Name the cell type shown.
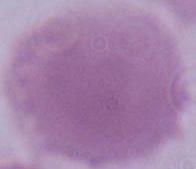

An erythrocyte.

Micrograph. Captured at 1000x magnification.